Outline each blood parasite and name the species.
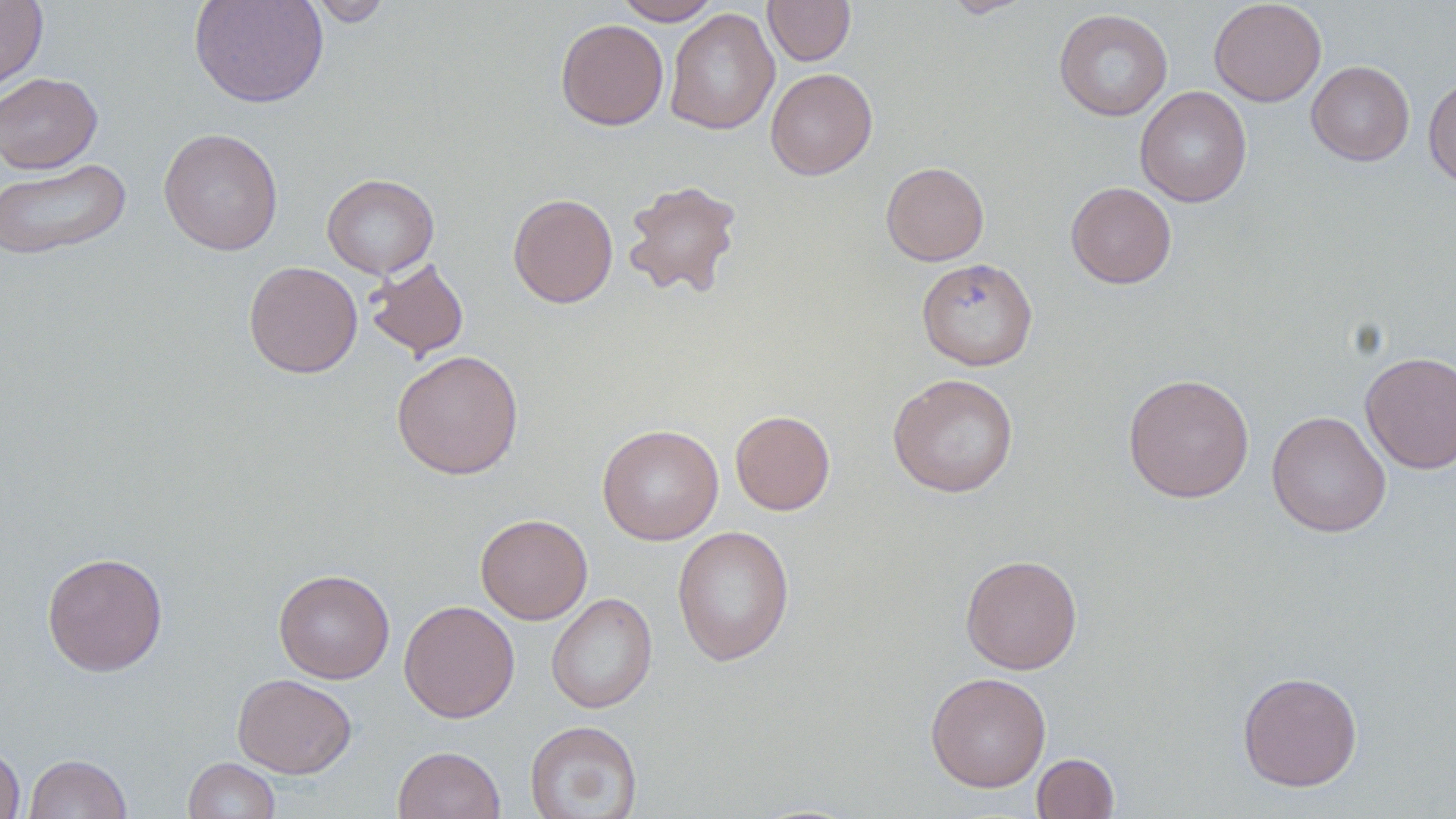
No blood parasites observed.

Summary:
  - Coordinate format: approximate bounding boxes as (x1,y1)-(x2,y2) corner pairs in pixels
  - Uninfected red blood cell locations: (0,0)-(48,93), (189,0)-(329,109), (308,0)-(393,26), (614,0)-(721,25), (763,0)-(855,66), (940,0)-(1033,18), (1209,0)-(1327,107), (665,8)-(779,135), (1053,8)-(1173,121), (555,19)-(668,130), (1307,61)-(1414,166), (765,68)-(878,180), (0,72)-(102,174), (1423,75)-(1456,188), (1135,86)-(1252,207), (158,127)-(283,255), (0,158)-(132,261), (881,161)-(989,266), (322,173)-(439,279), (622,179)-(743,300), (1065,181)-(1177,289), (507,193)-(618,308), (364,257)-(469,361), (917,257)-(1038,371), (243,261)-(362,378), (391,350)-(524,479), (1360,351)-(1456,474), (887,372)-(1019,498), (1122,373)-(1254,503), (730,410)-(835,515), (1266,410)-(1391,538), (597,424)-(724,545), (476,513)-(593,624), (672,525)-(795,667), (41,552)-(168,676), (960,554)-(1082,674), (273,569)-(395,683), (546,592)-(657,714), (399,599)-(520,723), (1237,670)-(1363,792), (925,671)-(1051,792), (232,673)-(357,778), (525,720)-(643,818), (0,743)-(25,819), (393,745)-(505,819), (1031,752)-(1120,818), (24,753)-(133,818), (183,757)-(281,819)
  - Slide-level diagnosis: no evidence of blood parasites
  - Image size: 1456×819 pixels
  - Field of view: single
  - Stain: May-Grünwald-Giemsa
  - Preparation: thin blood film
  - Magnification: 1000x
  - Modality: light microscopy